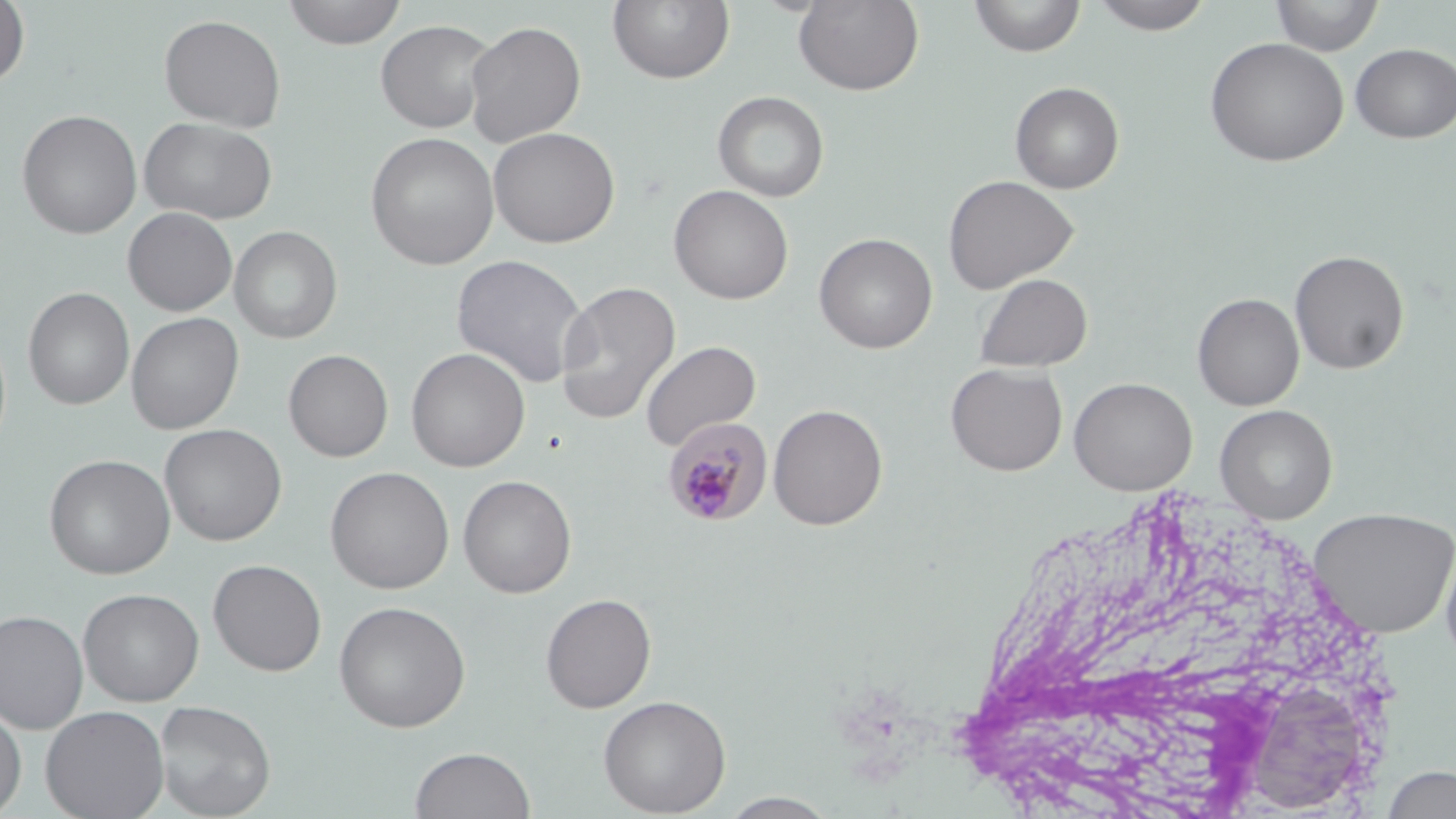

slide-level diagnosis = Plasmodium malariae
stain = May-Grünwald-Giemsa
image size = 1456×819 pixels
field of view = single
modality = light microscopy
preparation = thin blood film
Plasmodium malariae-infected red blood cell locations = approximate bounding boxes as (x1, y1, x2, y2) in pixels: (661, 417, 772, 528)
magnification = 1000x
uninfected red blood cell locations = approximate bounding boxes as (x1, y1, x2, y2) in pixels: (281, 0, 407, 49), (607, 0, 735, 85), (793, 0, 925, 96), (969, 0, 1086, 58), (1089, 0, 1216, 35), (1270, 0, 1385, 56), (0, 1, 31, 88), (158, 14, 286, 132), (375, 19, 496, 134), (465, 20, 586, 148), (1204, 37, 1349, 167), (1350, 43, 1456, 143), (1009, 82, 1124, 194), (712, 90, 829, 202), (17, 109, 142, 239), (139, 117, 277, 224), (488, 126, 620, 248), (365, 132, 500, 270), (943, 174, 1079, 294), (669, 184, 793, 304), (122, 207, 237, 316), (229, 226, 343, 344), (814, 232, 938, 354), (1290, 250, 1410, 374), (451, 253, 591, 389), (974, 273, 1092, 372), (554, 280, 681, 427), (23, 288, 134, 411), (1192, 293, 1304, 411), (126, 312, 244, 434), (639, 339, 762, 452), (406, 347, 530, 472), (283, 349, 394, 462), (945, 362, 1068, 476), (1068, 376, 1198, 496), (768, 403, 888, 530), (1215, 404, 1338, 523), (159, 424, 287, 546), (43, 453, 175, 580), (325, 466, 454, 594), (458, 475, 577, 598), (1308, 506, 1456, 639), (1438, 536, 1456, 668), (208, 559, 327, 676), (78, 588, 204, 706), (540, 593, 656, 713), (333, 601, 471, 732), (0, 609, 88, 733), (598, 694, 731, 817), (154, 699, 276, 818), (0, 702, 27, 817), (40, 705, 170, 819), (410, 746, 535, 819), (1381, 764, 1456, 818), (720, 792, 839, 818)